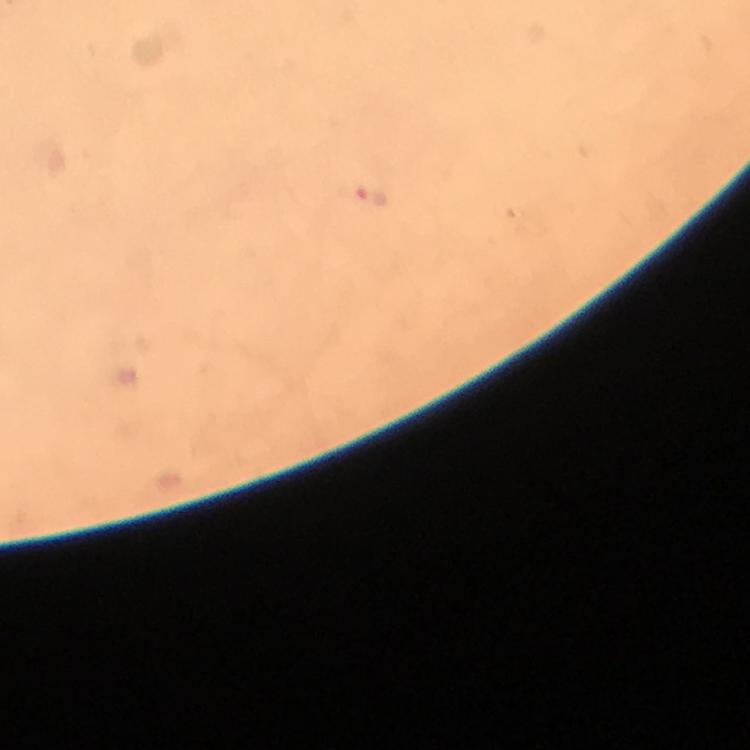

Approximate object centers, in pixels from the top-left corner.
Summary:
  - Plasmodium parasite locations: (x=370, y=198)
  - Magnification: 100x
  - Preparation: thick blood smear
  - Context: from a diagnostic examination for malaria
  - Capture: smartphone camera through the microscope
  - Cropped from: a single field of view
  - Immersion oil: used
  - Stain: Giemsa
  - Image size: 750×750 pixels